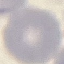

Malaria status: uninfected. Giemsa stain. Photographed with a smartphone camera at the microscope eyepiece. Thin smear of blood. Cell patch, automatically extracted from a larger field of view and resized to 64 × 64 pixels.